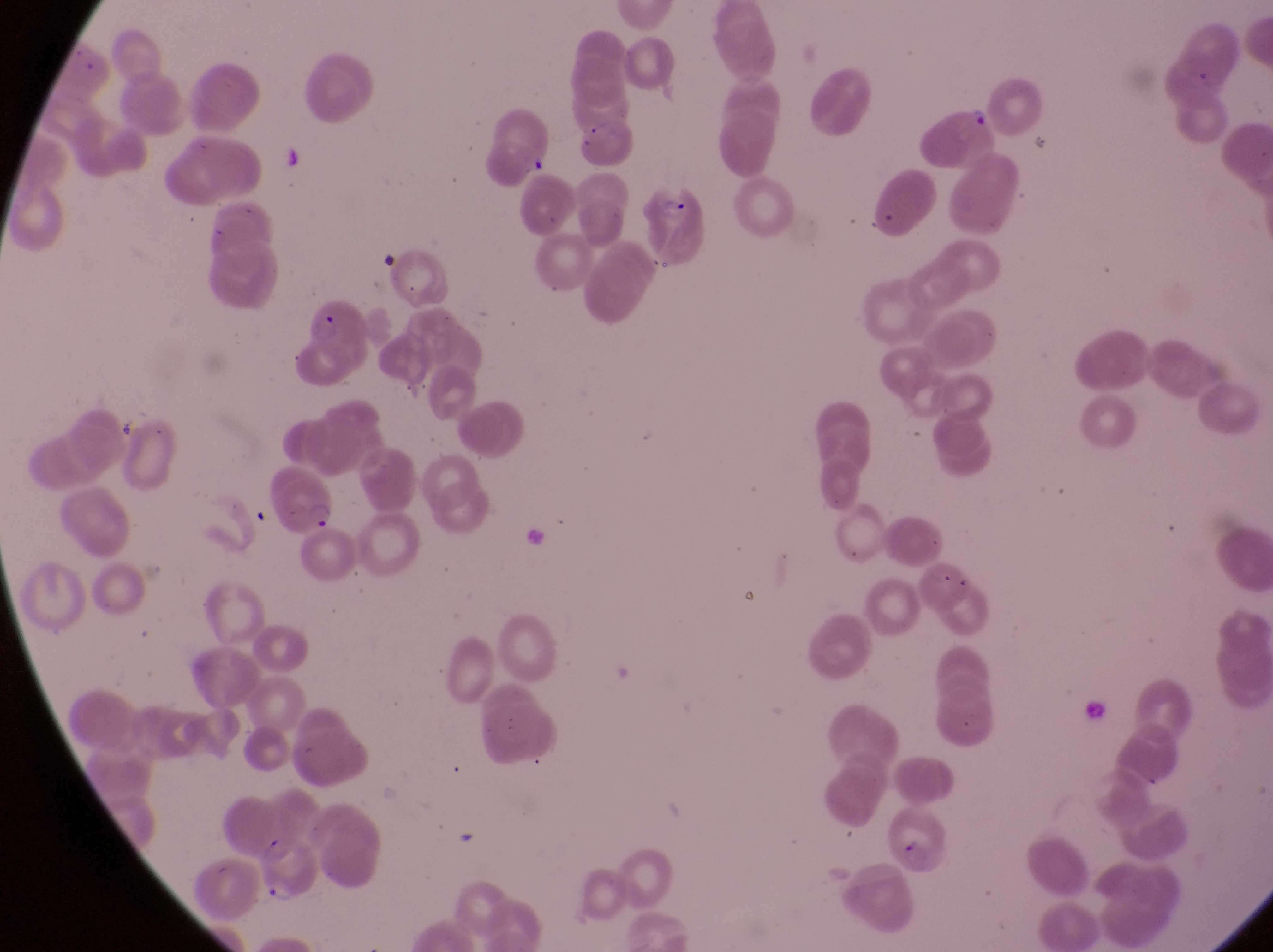
Approximate bounding boxes as [left, top, right, bottom] in pixels.
Summary:
  - Artifact (platelet-like body, stain precipitate, or debris) locations: [888, 810, 949, 873]
  - Parasitised red blood cell locations: [641, 178, 711, 268], [302, 289, 371, 377], [259, 464, 337, 536], [254, 834, 324, 901]
  - Trophozoite locations: [968, 107, 993, 134]
  - Capture: smartphone photograph through the eyepiece of an Olympus CX-23 microscope
  - Preparation: thin blood film
  - Field of view: single
  - Magnification: 1000x
  - Image size: 1273×952 pixels
  - Country: Uganda